Assess this cell for malaria.
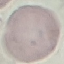
It is uninfected.

Thin smear of blood. Photographed with a smartphone camera at the microscope eyepiece. Automatically extracted cell patch, resized to 64 × 64 pixels. Giemsa-stained preparation.